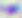

Summary:
  - Identification: Toxoplasma gondii
  - Magnification: 400x
  - Modality: photomicrograph